State the blood parasite species.
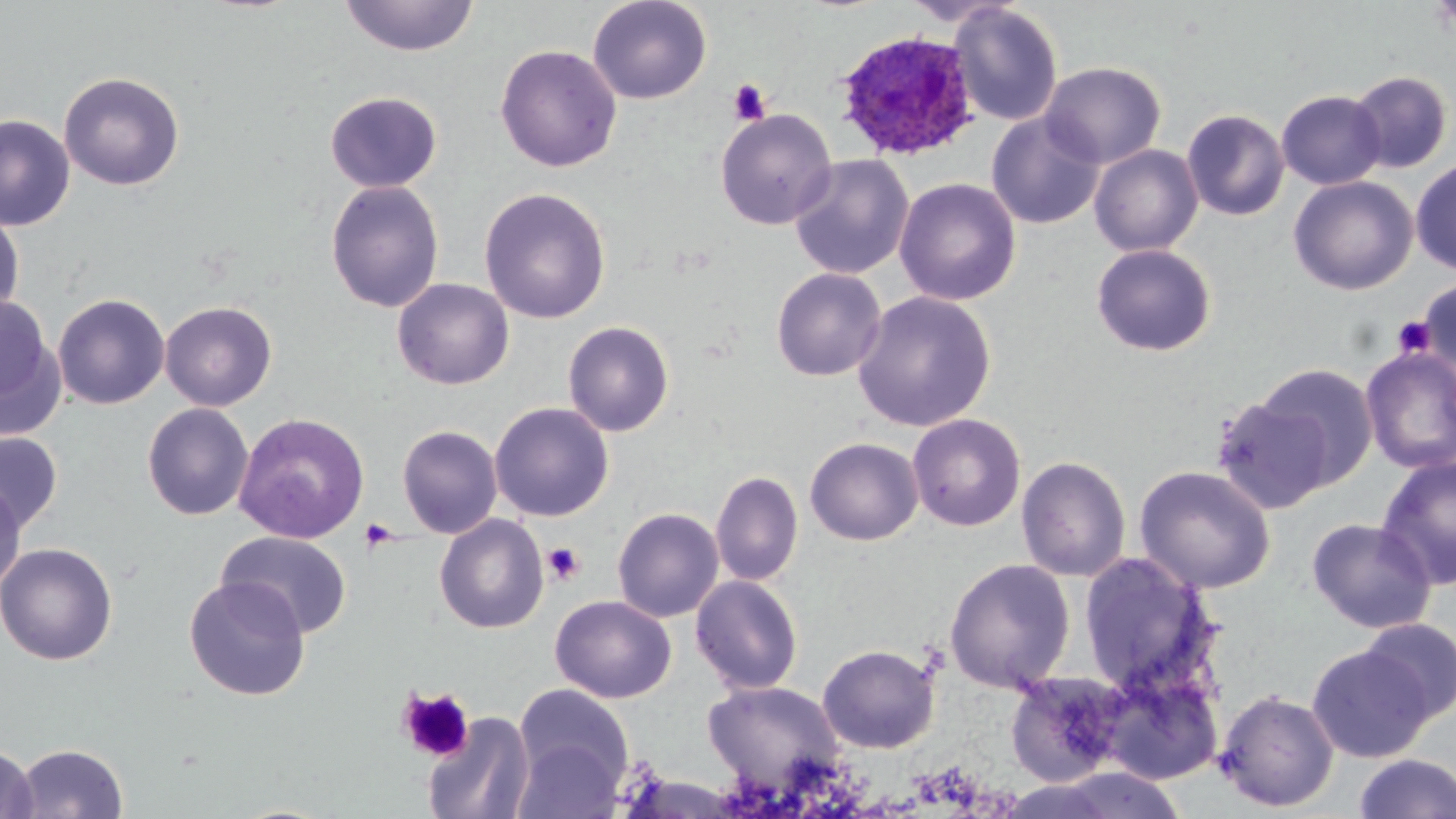
Plasmodium ovale.

Summary:
  - Coordinate format: approximate bounding boxes as named x1/y1/x2/y2 corners in pixels
  - Plasmodium ovale-infected red blood cell locations: (x1=831, y1=29, x2=982, y2=160)
  - Uninfected red blood cell locations: (x1=338, y1=0, x2=479, y2=56), (x1=588, y1=0, x2=712, y2=104), (x1=948, y1=3, x2=1063, y2=126), (x1=495, y1=44, x2=622, y2=173), (x1=1040, y1=61, x2=1167, y2=169), (x1=1347, y1=70, x2=1454, y2=174), (x1=58, y1=71, x2=185, y2=191), (x1=1276, y1=89, x2=1386, y2=190), (x1=324, y1=90, x2=442, y2=193), (x1=715, y1=108, x2=837, y2=229), (x1=1181, y1=108, x2=1290, y2=221), (x1=986, y1=112, x2=1105, y2=230), (x1=0, y1=114, x2=75, y2=231), (x1=1088, y1=144, x2=1204, y2=256), (x1=789, y1=154, x2=914, y2=279), (x1=1410, y1=157, x2=1456, y2=274), (x1=1288, y1=175, x2=1418, y2=295), (x1=894, y1=177, x2=1021, y2=306), (x1=325, y1=179, x2=445, y2=314), (x1=478, y1=186, x2=612, y2=324), (x1=0, y1=206, x2=25, y2=324), (x1=1090, y1=242, x2=1218, y2=357), (x1=770, y1=267, x2=887, y2=382), (x1=1416, y1=276, x2=1456, y2=376), (x1=392, y1=278, x2=514, y2=390), (x1=852, y1=290, x2=996, y2=433), (x1=0, y1=292, x2=63, y2=436), (x1=52, y1=293, x2=170, y2=409), (x1=160, y1=301, x2=278, y2=411), (x1=562, y1=321, x2=675, y2=437), (x1=1361, y1=347, x2=1456, y2=474), (x1=1252, y1=363, x2=1379, y2=490), (x1=1212, y1=395, x2=1333, y2=514), (x1=489, y1=402, x2=614, y2=522), (x1=141, y1=403, x2=254, y2=521), (x1=234, y1=412, x2=370, y2=544), (x1=907, y1=413, x2=1026, y2=532), (x1=397, y1=424, x2=503, y2=539), (x1=0, y1=431, x2=63, y2=534), (x1=804, y1=437, x2=924, y2=546), (x1=1016, y1=455, x2=1131, y2=583), (x1=1375, y1=455, x2=1456, y2=590), (x1=1134, y1=464, x2=1277, y2=595), (x1=710, y1=469, x2=803, y2=587), (x1=0, y1=478, x2=27, y2=594), (x1=612, y1=507, x2=724, y2=623), (x1=435, y1=515, x2=549, y2=634), (x1=1306, y1=517, x2=1436, y2=633), (x1=217, y1=531, x2=353, y2=639), (x1=0, y1=542, x2=118, y2=666), (x1=1077, y1=552, x2=1219, y2=696), (x1=944, y1=557, x2=1076, y2=692), (x1=690, y1=574, x2=804, y2=695), (x1=184, y1=576, x2=310, y2=701), (x1=550, y1=595, x2=677, y2=703), (x1=1357, y1=617, x2=1456, y2=724), (x1=817, y1=643, x2=941, y2=753), (x1=1306, y1=643, x2=1433, y2=762), (x1=1093, y1=661, x2=1224, y2=785), (x1=1005, y1=669, x2=1131, y2=787), (x1=702, y1=680, x2=845, y2=788), (x1=513, y1=683, x2=634, y2=802), (x1=1215, y1=688, x2=1340, y2=811), (x1=423, y1=711, x2=535, y2=819), (x1=512, y1=735, x2=623, y2=819), (x1=0, y1=743, x2=37, y2=819), (x1=12, y1=743, x2=129, y2=818), (x1=1352, y1=753, x2=1456, y2=819)
  - Platelet locations: (x1=727, y1=78, x2=772, y2=126), (x1=1392, y1=315, x2=1436, y2=358), (x1=360, y1=518, x2=400, y2=552), (x1=542, y1=542, x2=585, y2=585), (x1=398, y1=687, x2=474, y2=763)
  - Image size: 1456×819 pixels
  - Preparation: thin blood smear
  - Field of view: single
  - Stain: May-Grünwald-Giemsa
  - Magnification: 1000x
  - Modality: light microscopy